Classify this cell by malaria status.
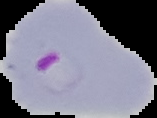
It is parasitized.

From a thin blood smear. Cell region segmented out of the field of view; the surrounding area is masked to black. Image is 157×118 pixels.